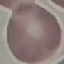

Summary:
  - Result: no malaria parasites seen
  - Preparation: thin blood smear
  - Image type: automatically extracted cell patch, resized to 64 × 64 pixels
  - Capture: smartphone camera at the microscope eyepiece
  - Stain: Giemsa